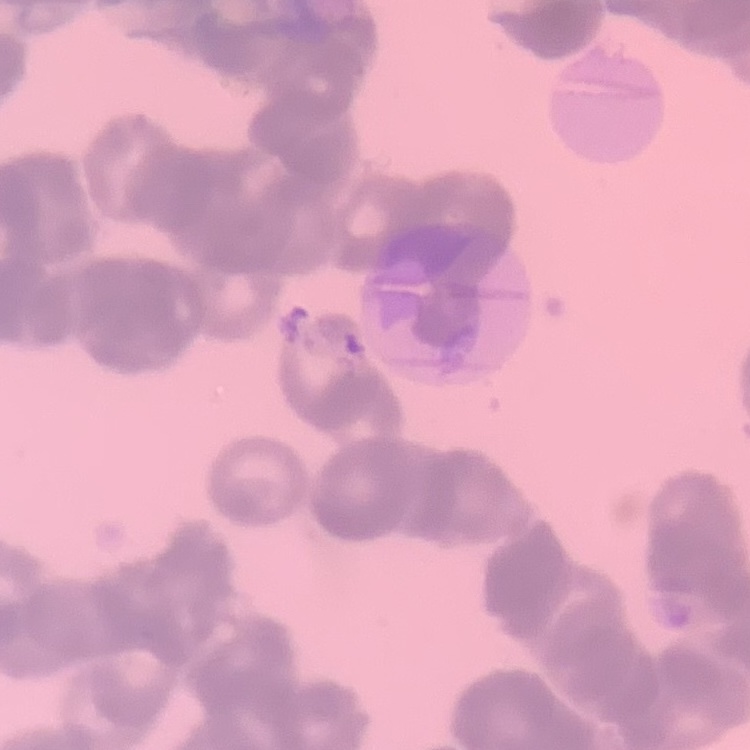
Summary:
  - Erythrocyte morphology: rouleaux formation
  - Image type: square crop of a larger photomicrograph
  - Preparation: thin peripheral smear
  - Stain: Field's or Giemsa